Report the malaria status of this cell.
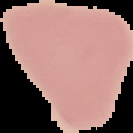

Uninfected.

Summary:
  - Image size: 133×133 pixels
  - Preparation: thin blood smear
  - Image type: segmented cell region on a black background